Name the parasite shown.
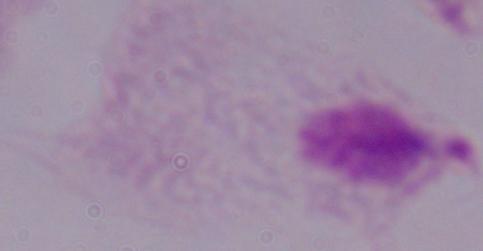
This is a trichomonad.

Summary:
  - Magnification: 1000x
  - Modality: photomicrograph